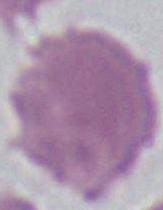

Micrograph. A red blood cell is seen. 1000x magnification.